Locate every Plasmodium falciparum-infected red blood cell.
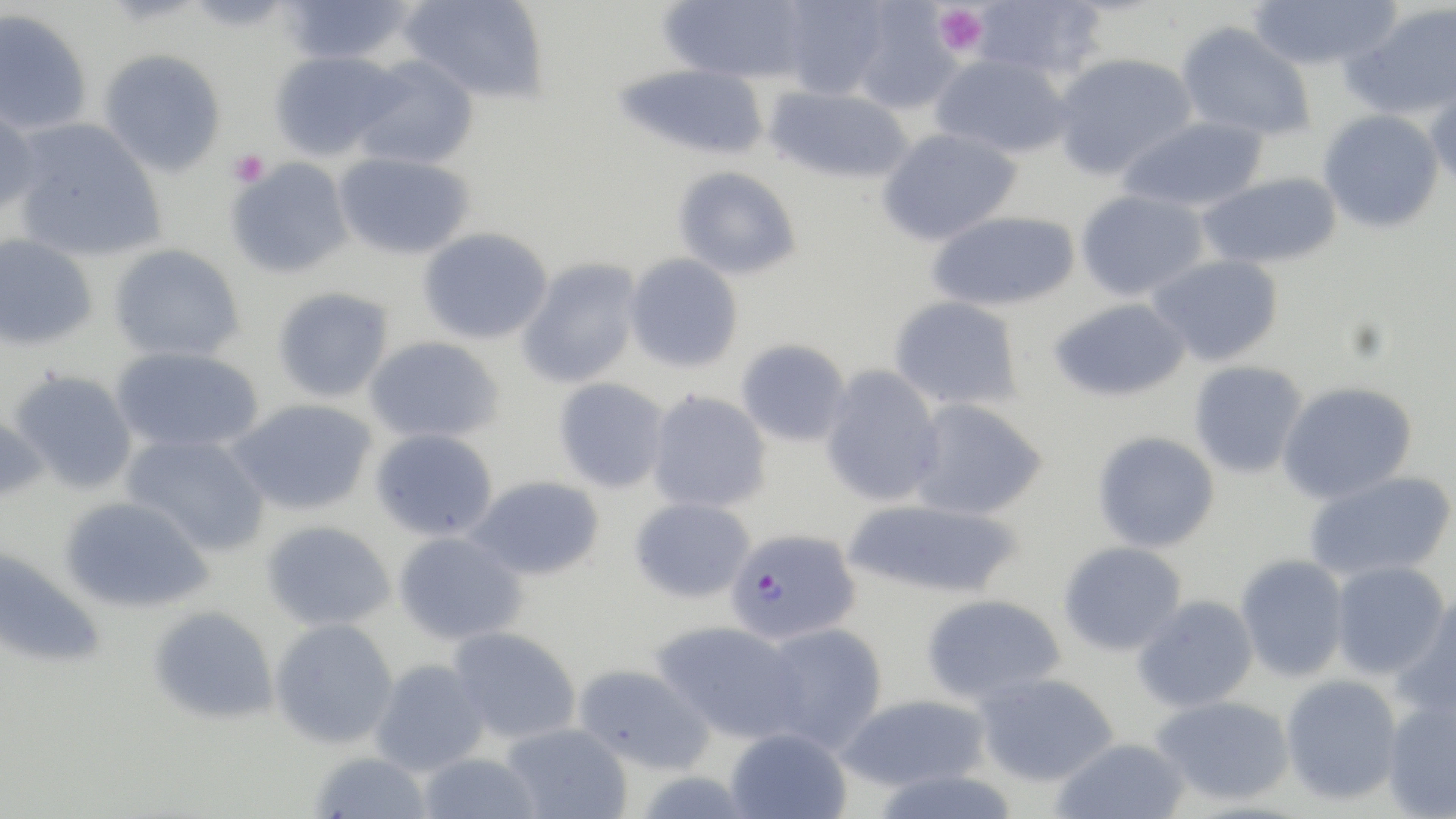
Approximate bounding boxes as named x1/y1/x2/y2 corners in pixels.
Plasmodium falciparum-infected red blood cells: (x1=727, y1=529, x2=862, y2=644).

Platelet locations: (x1=932, y1=3, x2=989, y2=57), (x1=228, y1=149, x2=269, y2=187). Uninfected red blood cell locations: (x1=399, y1=0, x2=550, y2=103), (x1=658, y1=0, x2=809, y2=84), (x1=778, y1=0, x2=891, y2=100), (x1=970, y1=0, x2=1106, y2=80), (x1=1247, y1=0, x2=1402, y2=71), (x1=278, y1=1, x2=416, y2=66), (x1=1341, y1=2, x2=1456, y2=121), (x1=849, y1=3, x2=963, y2=114), (x1=0, y1=8, x2=93, y2=135), (x1=1175, y1=21, x2=1316, y2=142), (x1=98, y1=49, x2=226, y2=177), (x1=268, y1=50, x2=401, y2=161), (x1=1051, y1=52, x2=1197, y2=180), (x1=930, y1=54, x2=1072, y2=157), (x1=351, y1=55, x2=479, y2=170), (x1=612, y1=63, x2=771, y2=161), (x1=1425, y1=81, x2=1456, y2=194), (x1=763, y1=85, x2=913, y2=185), (x1=0, y1=102, x2=42, y2=216), (x1=1318, y1=109, x2=1445, y2=233), (x1=1118, y1=115, x2=1269, y2=212), (x1=10, y1=119, x2=166, y2=262), (x1=877, y1=127, x2=1022, y2=246), (x1=333, y1=151, x2=475, y2=261), (x1=225, y1=156, x2=355, y2=280), (x1=672, y1=166, x2=802, y2=280), (x1=1196, y1=172, x2=1343, y2=269), (x1=1075, y1=189, x2=1209, y2=301), (x1=926, y1=210, x2=1082, y2=312), (x1=417, y1=227, x2=554, y2=345), (x1=0, y1=232, x2=99, y2=352), (x1=108, y1=243, x2=246, y2=363), (x1=624, y1=253, x2=744, y2=373), (x1=1148, y1=253, x2=1284, y2=367), (x1=516, y1=257, x2=643, y2=388), (x1=272, y1=286, x2=394, y2=402), (x1=889, y1=295, x2=1023, y2=410), (x1=1048, y1=297, x2=1191, y2=402), (x1=364, y1=336, x2=504, y2=444), (x1=736, y1=338, x2=851, y2=447), (x1=110, y1=346, x2=263, y2=454), (x1=1188, y1=360, x2=1308, y2=478), (x1=819, y1=365, x2=945, y2=507), (x1=9, y1=369, x2=139, y2=494), (x1=553, y1=377, x2=670, y2=493), (x1=1277, y1=380, x2=1418, y2=504), (x1=646, y1=390, x2=772, y2=513), (x1=908, y1=397, x2=1048, y2=520), (x1=227, y1=398, x2=379, y2=516), (x1=0, y1=413, x2=52, y2=504), (x1=368, y1=428, x2=499, y2=542), (x1=1092, y1=430, x2=1221, y2=553), (x1=120, y1=433, x2=271, y2=557), (x1=1303, y1=470, x2=1456, y2=582), (x1=466, y1=475, x2=606, y2=582), (x1=58, y1=496, x2=214, y2=614), (x1=629, y1=497, x2=755, y2=603), (x1=842, y1=498, x2=1024, y2=599), (x1=261, y1=520, x2=395, y2=631), (x1=392, y1=531, x2=529, y2=645), (x1=1058, y1=541, x2=1187, y2=655), (x1=0, y1=545, x2=107, y2=668), (x1=1235, y1=553, x2=1349, y2=683), (x1=1329, y1=560, x2=1449, y2=680), (x1=1390, y1=593, x2=1456, y2=720), (x1=921, y1=594, x2=1066, y2=705), (x1=1132, y1=595, x2=1259, y2=712), (x1=148, y1=605, x2=279, y2=725), (x1=269, y1=618, x2=398, y2=749), (x1=653, y1=620, x2=806, y2=742), (x1=759, y1=622, x2=888, y2=753), (x1=447, y1=626, x2=581, y2=744), (x1=370, y1=658, x2=490, y2=776), (x1=574, y1=663, x2=715, y2=775), (x1=974, y1=672, x2=1118, y2=787), (x1=1280, y1=674, x2=1403, y2=804), (x1=835, y1=692, x2=992, y2=793), (x1=1151, y1=694, x2=1295, y2=806), (x1=1381, y1=701, x2=1456, y2=818), (x1=500, y1=722, x2=632, y2=818), (x1=724, y1=727, x2=852, y2=818), (x1=1050, y1=737, x2=1192, y2=819), (x1=309, y1=752, x2=432, y2=819), (x1=417, y1=752, x2=543, y2=819). Slide-level diagnosis: Plasmodium falciparum. Image is 1456×819 pixels. Thin blood film. Optical microscopy. May-Grünwald-Giemsa-stained preparation. Single field of view. 1000x magnification.